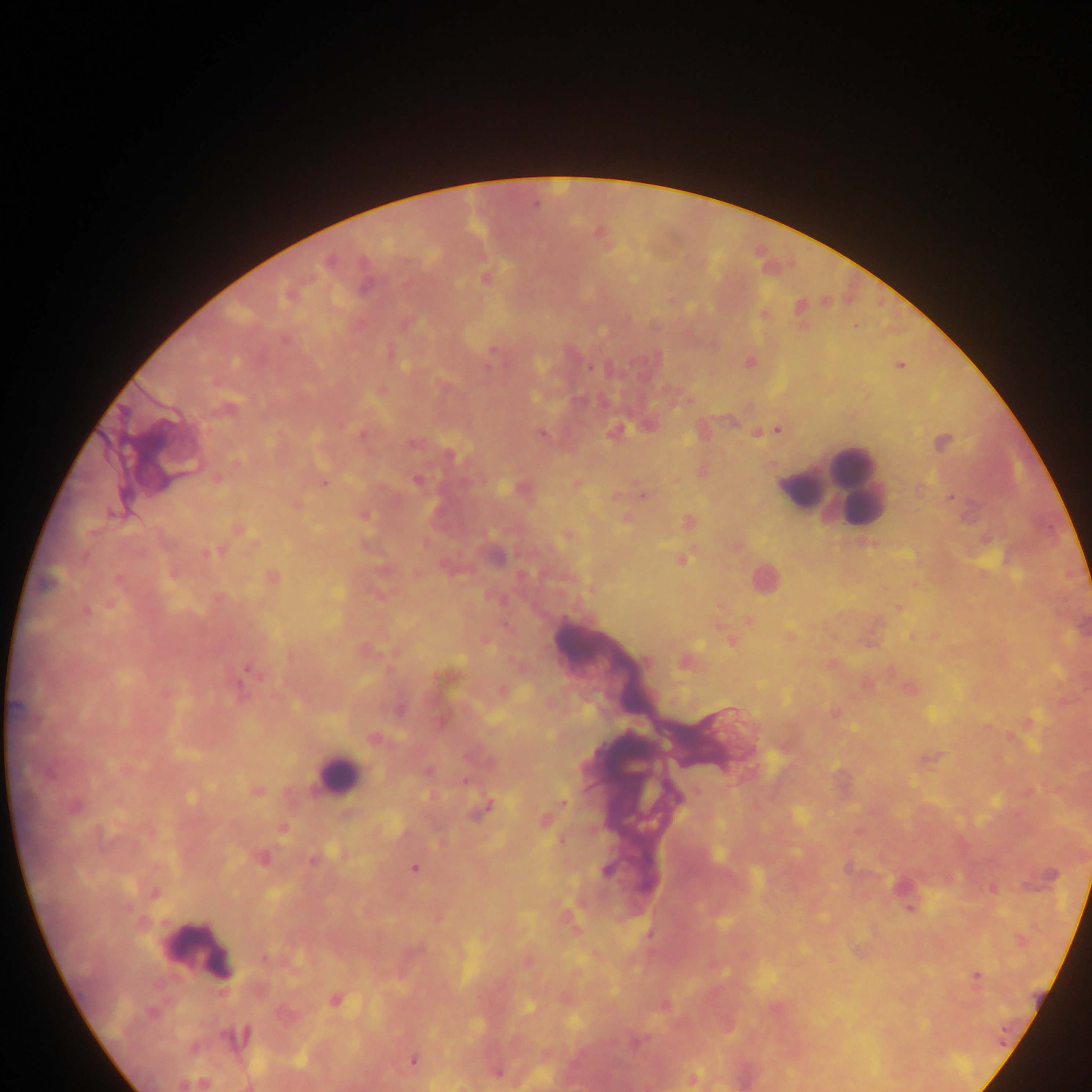

Approximate centers as x y in pixels.
Summary:
  - Plasmodium parasite locations: 535 204; 598 232; 328 261; 486 278; 799 306; 284 340; 493 350; 489 366; 900 366; 589 367; 382 390; 777 430; 541 434; 361 435; 412 444; 236 463; 218 479; 417 481; 323 483; 643 496; 951 497; 298 506; 239 528; 568 535; 206 553; 273 577; 110 603; 898 607; 85 611; 749 621; 731 641; 646 661; 248 670; 835 713; 373 739; 428 770; 49 773; 465 781; 258 791; 698 792; 564 802; 488 806; 75 807; 282 829; 561 840; 262 857; 312 861; 414 868; 606 871; 155 893; 910 910; 264 957; 977 976; 335 1001; 151 1012; 237 1037; 413 1060; 498 1072; 694 1077
  - Leukocyte locations: 851 468; 829 486; 803 489; 764 578; 336 773; 200 950
  - Preparation: thick blood film
  - Image size: 1092×1092 pixels
  - Capture: mobile-phone photograph through a microscope
  - Country: Ghana
  - Field of view: single